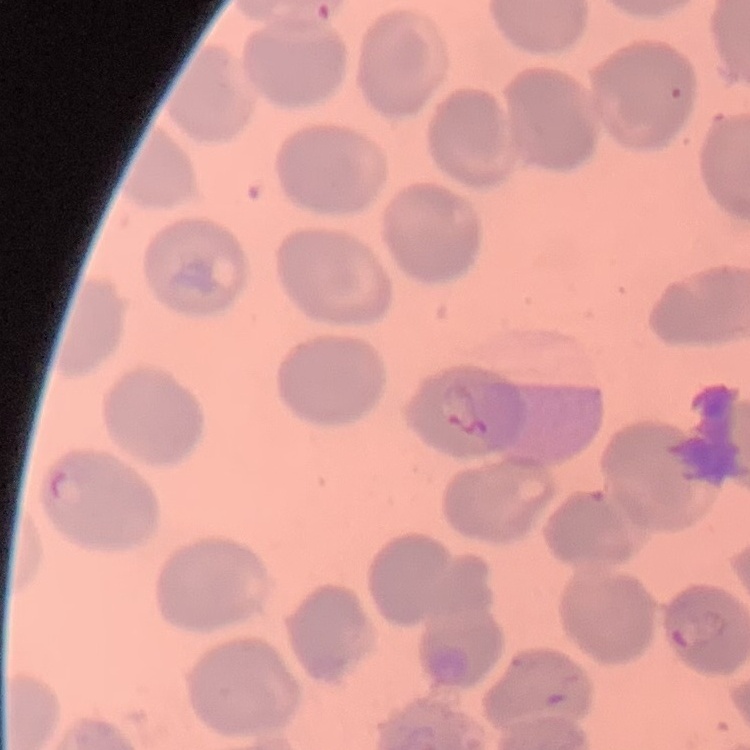

Summary:
  - Red blood cell morphology: no rouleaux formation
  - Image type: square crop of a larger photomicrograph
  - Stain: Field's or Giemsa
  - Preparation: thin blood film